State which cell type is depicted.
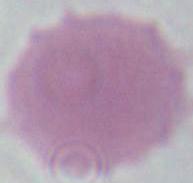
This is an erythrocyte.

modality = photomicrograph
magnification = 1000x